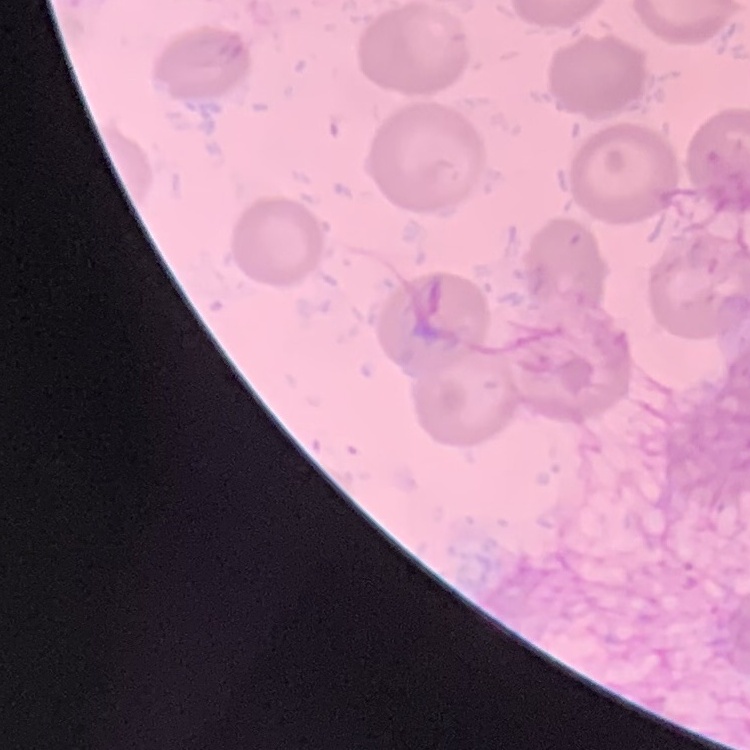

Summary:
  - Red blood cell morphology: no rouleaux formation
  - Image type: square crop of a larger photomicrograph
  - Preparation: thin blood film
  - Stain: Field's or Giemsa